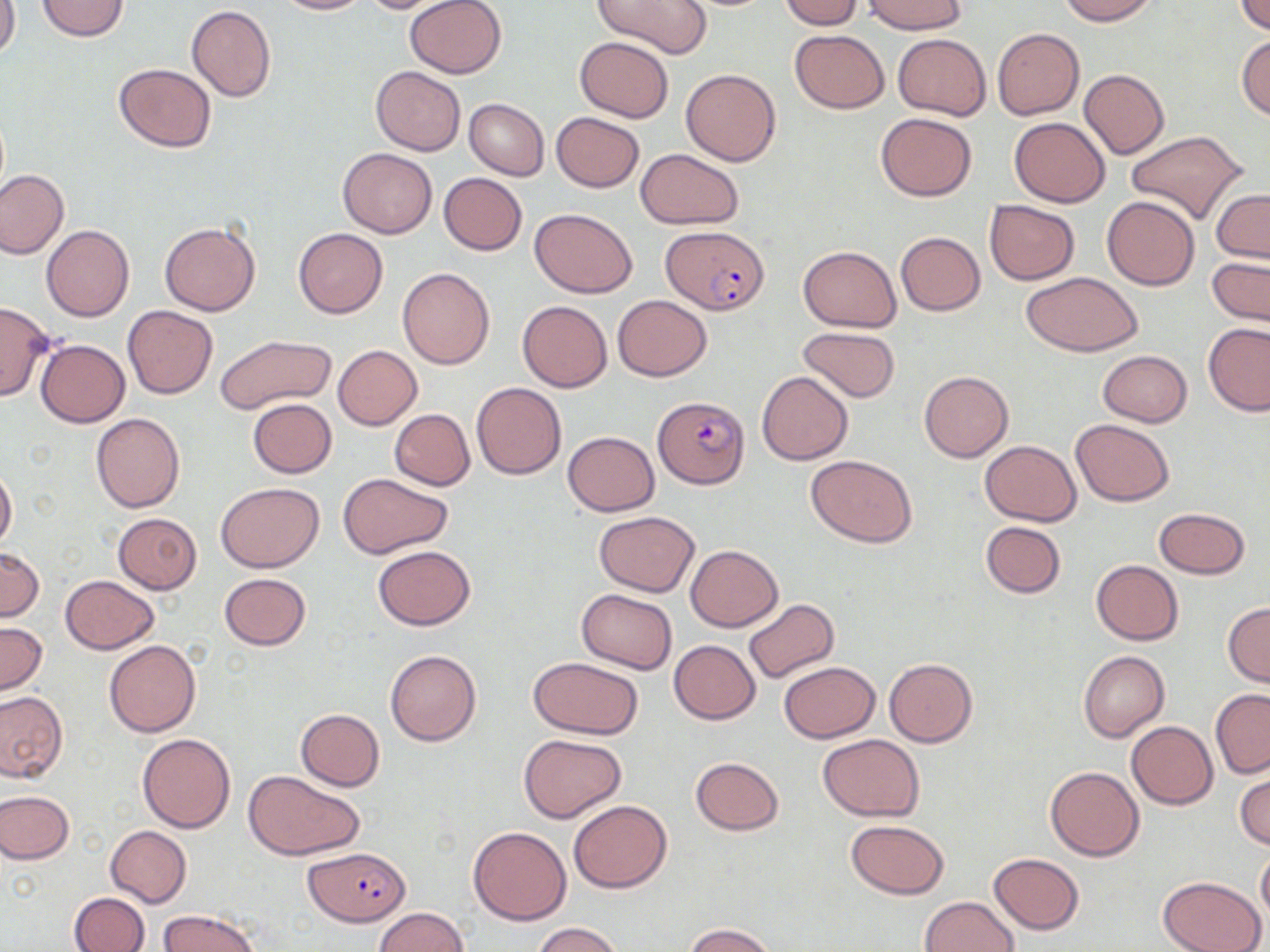

Approximate bounding boxes as [x1, y1, x2, y2] in pixels. Uninfected red blood cell locations: [0, 0, 20, 64], [35, 0, 130, 42], [275, 0, 368, 15], [357, 0, 456, 14], [405, 0, 506, 79], [593, 0, 713, 60], [779, 0, 863, 29], [1055, 0, 1158, 25], [1235, 0, 1270, 35], [863, 1, 967, 34], [187, 4, 276, 101], [992, 28, 1084, 120], [789, 29, 890, 113], [893, 33, 990, 119], [1237, 35, 1270, 121], [575, 37, 673, 122], [113, 63, 217, 152], [370, 66, 464, 155], [681, 69, 781, 166], [1078, 69, 1170, 159], [463, 99, 549, 180], [550, 112, 645, 192], [875, 113, 977, 200], [1008, 117, 1111, 207], [1125, 130, 1249, 225], [337, 148, 437, 239], [636, 149, 743, 228], [0, 169, 69, 258], [438, 173, 526, 255], [1211, 189, 1269, 263], [1102, 196, 1200, 290], [983, 201, 1080, 285], [530, 209, 637, 297], [160, 222, 260, 315], [42, 225, 135, 322], [294, 228, 388, 318], [895, 232, 985, 316], [800, 246, 901, 331], [1208, 257, 1269, 326], [397, 267, 495, 368], [1021, 271, 1144, 356], [612, 295, 712, 381], [0, 301, 53, 402], [517, 301, 613, 391], [124, 305, 217, 399], [1202, 322, 1270, 415], [798, 325, 901, 403], [215, 335, 337, 412], [35, 338, 130, 426], [333, 345, 422, 430], [1098, 350, 1192, 427], [756, 370, 853, 464], [919, 371, 1013, 462], [471, 383, 566, 479], [247, 398, 337, 478], [390, 408, 474, 490], [90, 413, 185, 513], [1070, 420, 1175, 507], [562, 431, 659, 514], [979, 440, 1082, 525], [806, 454, 917, 547], [0, 465, 17, 551], [340, 472, 452, 559], [217, 482, 323, 573], [1154, 507, 1251, 579], [1117, 509, 1238, 610], [594, 511, 700, 595], [114, 512, 201, 593], [979, 521, 1065, 598], [687, 545, 782, 630], [0, 546, 43, 621], [372, 546, 476, 630], [1091, 560, 1183, 644], [218, 573, 311, 651], [60, 576, 159, 653], [575, 589, 677, 673], [742, 597, 838, 684], [1224, 602, 1270, 686], [0, 621, 47, 697], [669, 639, 760, 724], [104, 640, 201, 736], [385, 649, 481, 746], [1078, 651, 1169, 741], [529, 656, 643, 738], [883, 658, 977, 747], [779, 661, 880, 743], [1211, 690, 1270, 779], [0, 691, 67, 782], [295, 708, 385, 791], [1126, 721, 1219, 809], [137, 733, 235, 833], [519, 733, 626, 822], [819, 734, 924, 821], [690, 756, 784, 835], [1044, 766, 1145, 861], [245, 770, 366, 861], [1235, 770, 1270, 851], [0, 792, 74, 864], [568, 800, 673, 893], [844, 819, 949, 899], [104, 826, 191, 907], [468, 826, 571, 925], [1256, 848, 1270, 925], [989, 853, 1083, 935], [1157, 876, 1266, 952], [68, 892, 149, 952], [918, 896, 1018, 952], [374, 908, 467, 952], [159, 910, 262, 952], [530, 922, 625, 952], [684, 923, 774, 952]. Plasmodium falciparum-infected red blood cell locations: [662, 226, 769, 314], [653, 395, 750, 490], [303, 847, 412, 925]. Slide-level diagnosis: Plasmodium falciparum. Single field of view. May-Grünwald-Giemsa stain. Light microscopy. Thin blood smear. 1000x magnification. Image is 1270×952 pixels.